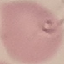

malaria status = parasitized
capture = smartphone camera at the microscope eyepiece
preparation = thin blood smear
image type = cell patch, automatically extracted from a larger field of view and resized to 64 × 64 pixels
stain = Giemsa